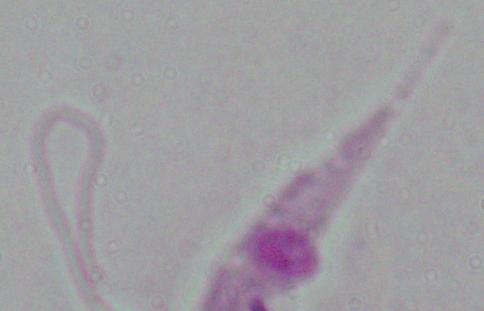

Summary:
  - Magnification: 1000x
  - Modality: photomicrograph
  - Identification: Leishmania